Give the preparation type.
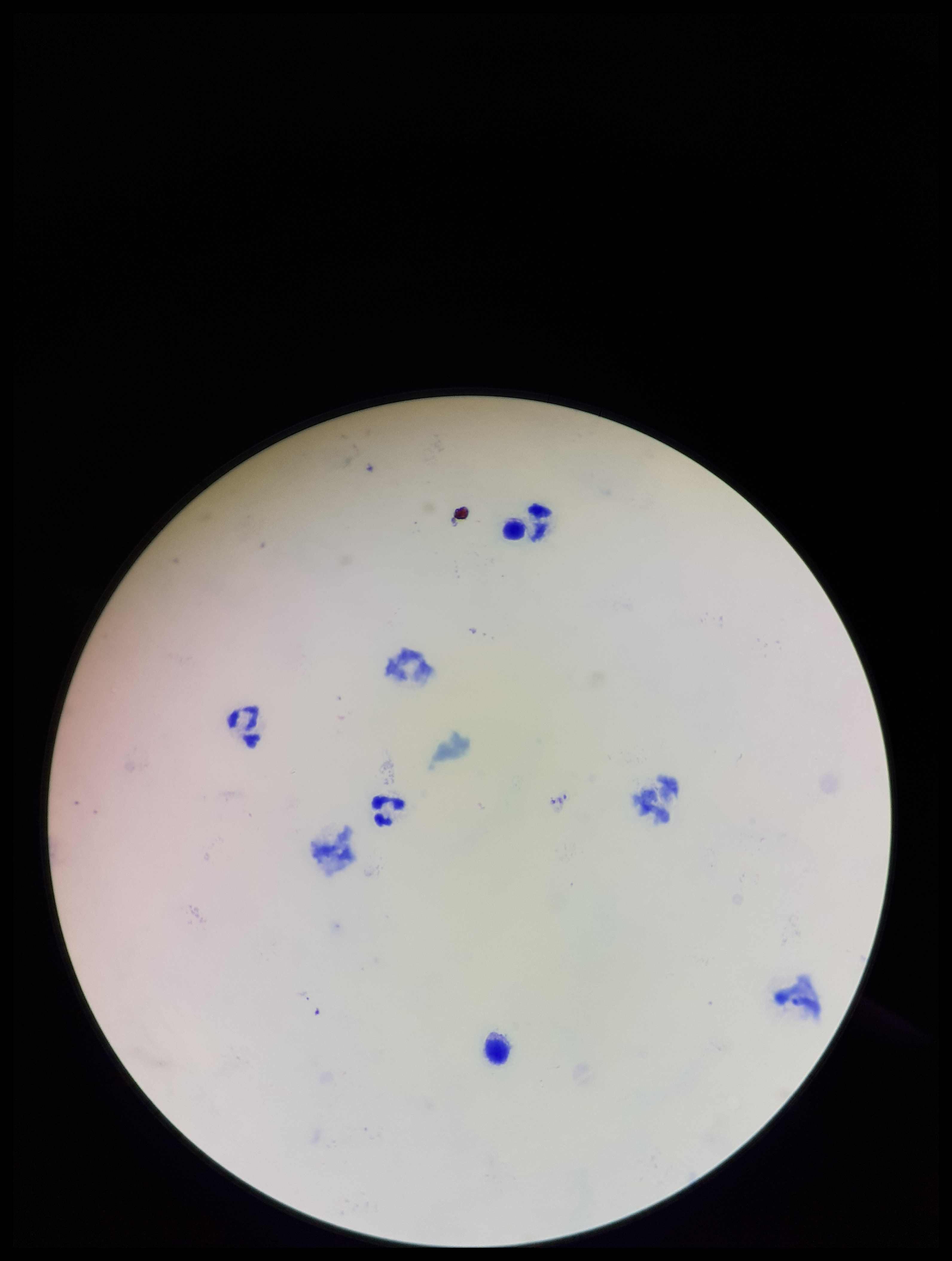
A thick smear.

field_of_view: one from this slide
capture: smartphone photograph through the microscope eyepiece
leukocyte_count: 4
parasite_count: 0
image_size: 952×1261 pixels
plasmodium_parasites: none identified
stain: Giemsa
patient_malaria_status: negative